State which cell type is depicted.
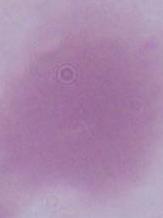

An erythrocyte.

modality = photomicrograph
magnification = 1000x